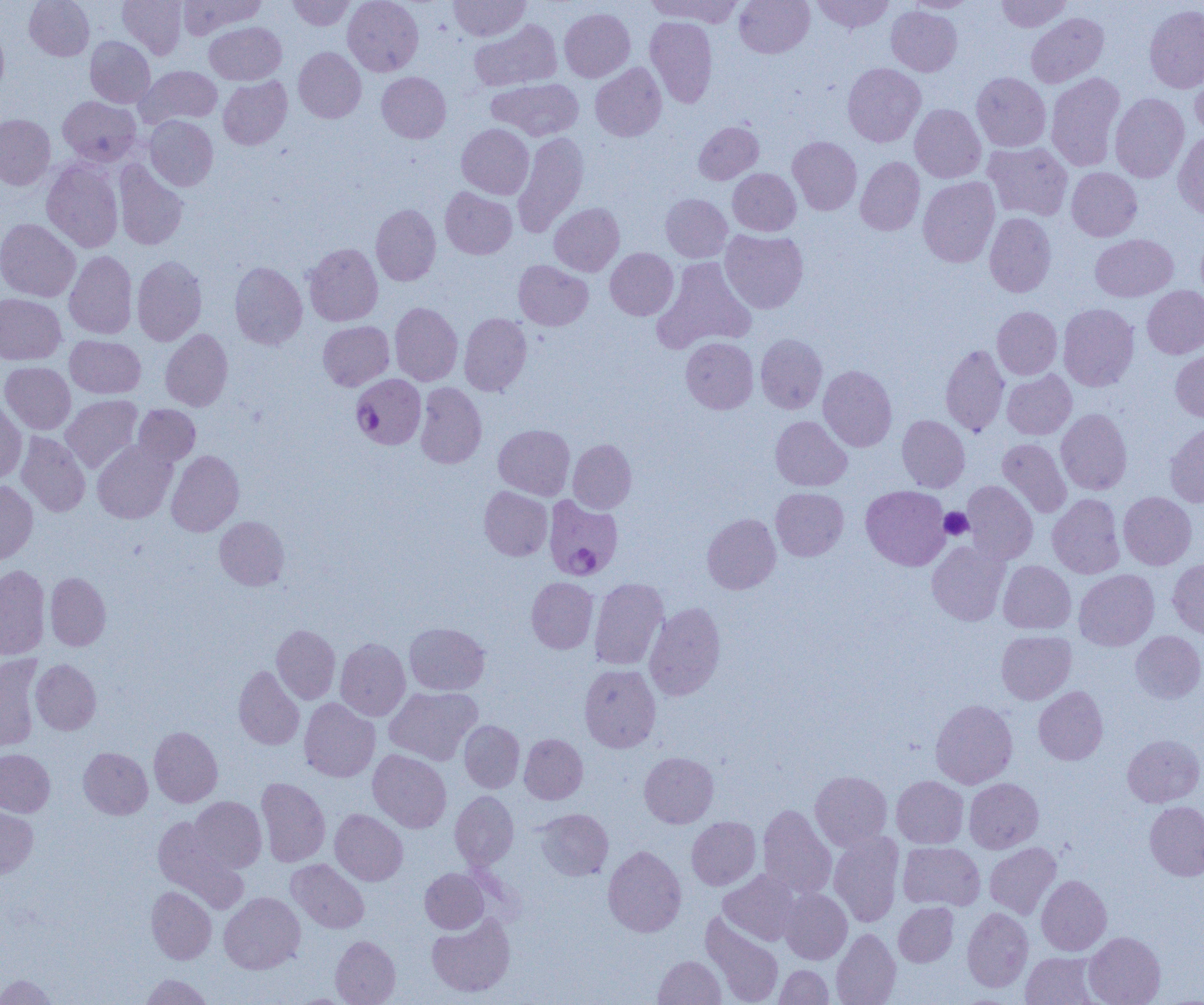
Summary:
  - Coordinate format: approximate bounding boxes as (x1,y1)-(x2,y2) corner pairs in pixels
  - Platelet locations: (940,508)-(973,540)
  - Uninfected red blood cell locations: (24,0)-(94,60), (117,0)-(187,60), (178,0)-(266,38), (287,0)-(355,30), (343,0)-(423,76), (449,0)-(531,41), (646,0)-(742,26), (734,0)-(814,58), (811,0)-(894,33), (907,0)-(978,13), (996,0)-(1072,32), (1144,5)-(1204,93), (886,6)-(962,76), (559,8)-(635,82), (1026,13)-(1109,87), (645,16)-(717,108), (469,20)-(562,91), (205,22)-(286,84), (0,23)-(9,98), (85,36)-(155,107), (293,47)-(366,123), (842,62)-(925,147), (590,63)-(666,141), (1191,64)-(1204,141), (136,65)-(222,128), (377,72)-(451,143), (971,72)-(1051,151), (1046,73)-(1125,171), (218,76)-(292,149), (489,78)-(584,141), (1110,93)-(1189,183), (58,96)-(141,166), (910,104)-(986,183), (0,114)-(55,190), (145,115)-(218,190), (694,121)-(763,184), (457,124)-(534,199), (1173,130)-(1204,219), (513,132)-(588,236), (788,136)-(862,215), (983,142)-(1073,220), (856,157)-(925,235), (42,160)-(123,253), (113,161)-(188,250), (1066,167)-(1142,241), (728,168)-(801,235), (918,177)-(999,267), (440,187)-(517,259), (660,194)-(732,262), (550,203)-(624,276), (371,204)-(441,286), (985,212)-(1056,297), (0,219)-(80,302), (1196,228)-(1204,305), (720,229)-(808,313), (1090,234)-(1177,301), (303,243)-(383,326), (605,248)-(678,320), (64,251)-(137,339), (132,255)-(207,345), (652,256)-(757,353), (514,260)-(593,330), (229,261)-(307,350), (1142,285)-(1204,358), (0,293)-(66,364), (390,302)-(462,385), (1058,303)-(1139,391), (992,306)-(1062,379), (459,313)-(531,396), (318,321)-(394,390), (160,329)-(233,411), (755,334)-(827,414), (65,335)-(145,398), (681,337)-(758,413), (940,344)-(1009,436), (1170,348)-(1204,422), (0,362)-(75,434), (818,365)-(897,451), (1002,370)-(1076,440), (415,382)-(486,468), (61,395)-(142,473), (0,399)-(26,482), (134,404)-(200,467), (1056,409)-(1132,494), (897,415)-(970,492), (771,416)-(852,491), (1164,421)-(1204,508), (494,424)-(575,499), (16,432)-(90,517), (997,438)-(1072,518), (92,439)-(177,524), (568,439)-(636,513), (166,450)-(244,536), (962,480)-(1038,564), (0,481)-(38,563), (861,485)-(951,570), (479,486)-(552,560), (771,488)-(848,560), (1118,492)-(1196,570), (1047,493)-(1125,578), (702,513)-(780,594), (214,516)-(289,590), (927,541)-(1010,626), (1168,558)-(1204,640), (998,560)-(1075,634), (0,565)-(50,659), (1074,569)-(1159,651), (45,572)-(111,651), (527,577)-(598,653), (589,578)-(669,670), (645,602)-(726,700), (404,622)-(489,695), (272,625)-(340,704), (996,630)-(1076,704), (1130,631)-(1204,703), (335,638)-(410,720), (0,654)-(43,752), (30,659)-(101,734), (579,664)-(661,752), (234,665)-(304,750), (384,686)-(481,765), (1033,686)-(1108,765), (299,698)-(379,781), (930,699)-(1018,788), (460,720)-(525,792), (149,726)-(222,807), (519,734)-(588,804), (1123,734)-(1204,807), (78,747)-(152,819), (0,749)-(55,817), (368,749)-(451,832), (640,752)-(719,828), (810,771)-(892,850), (892,776)-(968,848), (256,777)-(330,867), (964,778)-(1043,853), (450,791)-(518,869), (189,796)-(266,872), (1145,801)-(1204,881), (758,804)-(836,900), (0,806)-(38,879), (536,808)-(613,881), (330,809)-(408,885), (152,815)-(248,912), (687,816)-(760,890), (829,832)-(904,927), (899,842)-(985,910), (985,842)-(1061,919), (603,845)-(686,937), (287,859)-(369,933), (420,868)-(488,933), (719,870)-(800,945), (1036,875)-(1111,955), (146,886)-(216,964), (780,888)-(852,964), (219,892)-(305,973), (893,902)-(959,966), (962,907)-(1033,992), (427,913)-(515,997), (701,913)-(783,1005), (831,928)-(901,1005), (1084,931)-(1165,1005), (330,935)-(400,1005), (1021,951)-(1100,1005), (653,955)-(726,1005), (774,965)-(834,1004), (1,974)-(57,1004), (141,974)-(213,1004), (288,994)-(356,1005)
  - Plasmodium falciparum-infected red blood cell locations: (351,374)-(426,450), (544,497)-(624,581)
  - Slide-level diagnosis: Plasmodium falciparum
  - Image size: 1204×1005 pixels
  - Preparation: thin blood film
  - Magnification: 1000x
  - Field of view: single
  - Modality: optical microscopy